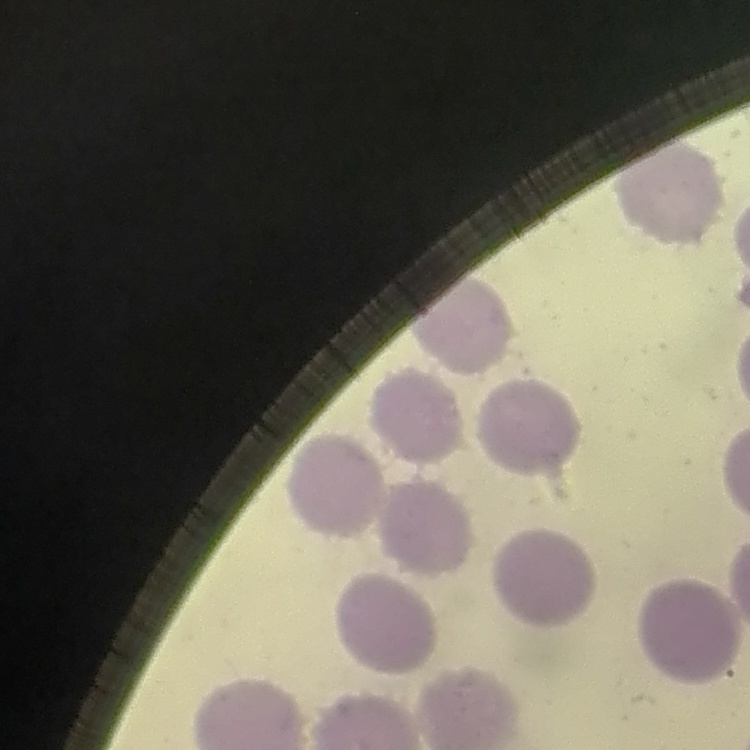

Summary:
  - Red blood cell morphology: no rouleaux formation
  - Stain: Field's or Giemsa
  - Image type: one tile cut from a larger photomicrograph
  - Preparation: thin peripheral smear